State the preparation type.
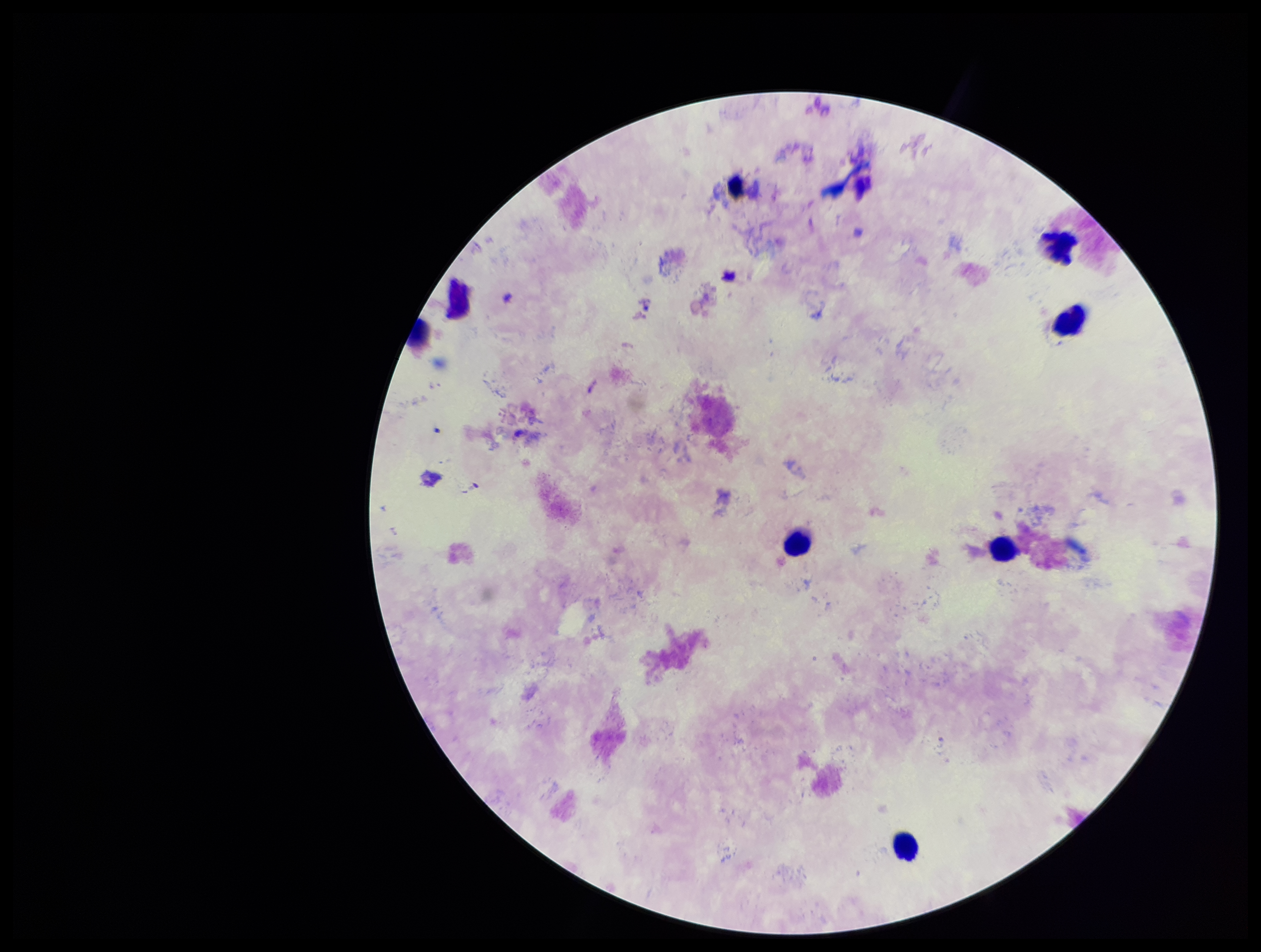

It is a thick blood smear.

Leukocyte count: 5. Image is 1261×952 pixels. One field from this slide. Patient malaria status: positive. Species reported for this patient: Plasmodium falciparum. Smartphone photograph taken through the eyepiece of a microscope. Plasmodium parasites: none detected. Giemsa stain. Parasite count: 0.